Report the malaria status of this cell.
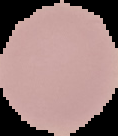

It is uninfected.

Image is 118×136 pixels. From a thin blood film. Cell region segmented out of the field of view; the surrounding area is masked to black.